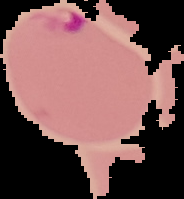
image size = 184×199 pixels
malaria status = parasitized
preparation = thin blood film
image type = cell region segmented out of the field of view; surrounding area masked to black